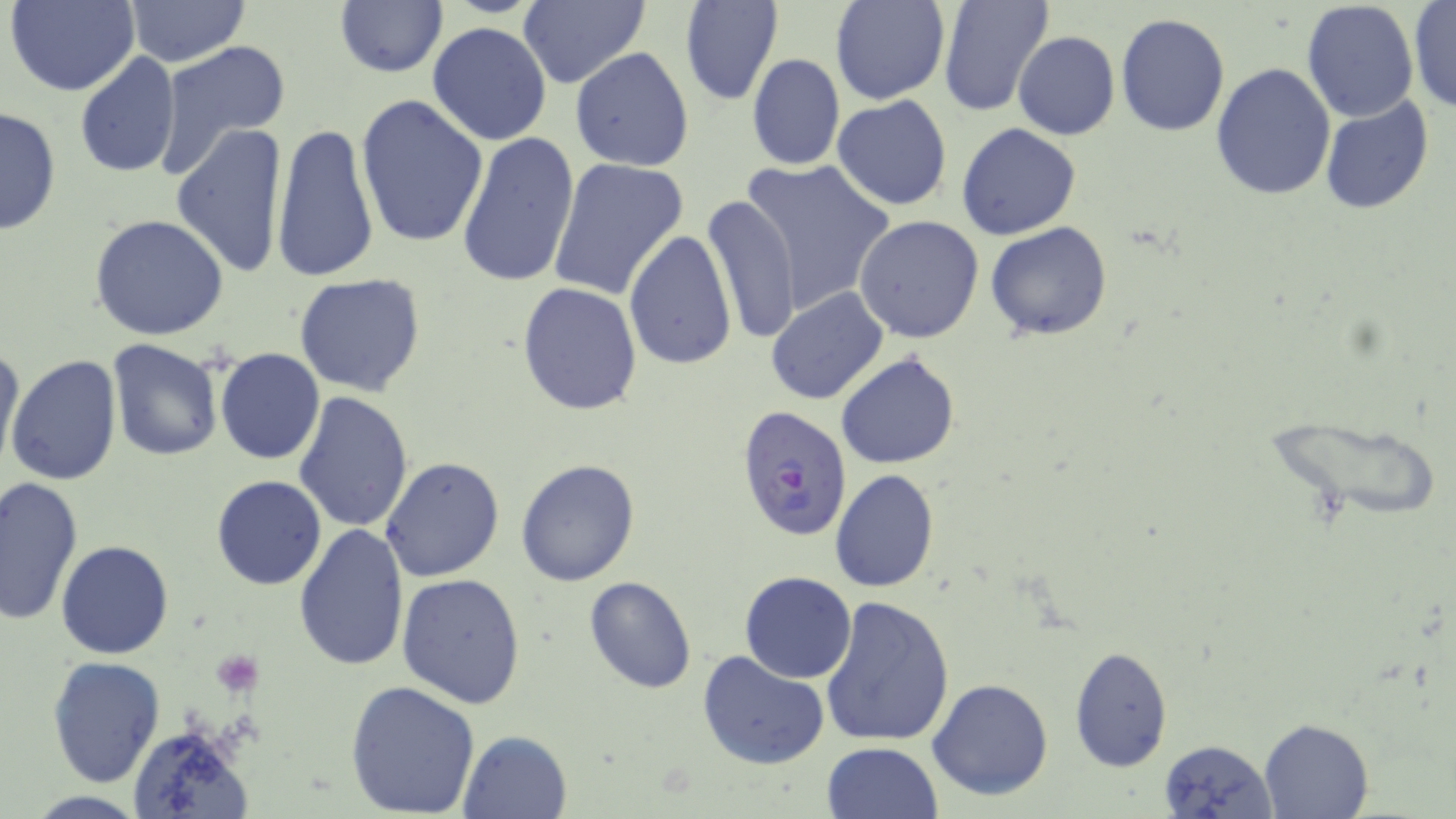

Summary:
  - Coordinate format: approximate bounding boxes as named x1/y1/x2/y2 corners in pixels
  - Plasmodium falciparum-infected red blood cell locations: (x1=734, y1=404, x2=854, y2=543)
  - Uninfected red blood cell locations: (x1=5, y1=0, x2=139, y2=96), (x1=125, y1=0, x2=248, y2=67), (x1=334, y1=0, x2=448, y2=79), (x1=680, y1=0, x2=784, y2=107), (x1=830, y1=0, x2=950, y2=105), (x1=937, y1=0, x2=1055, y2=117), (x1=1301, y1=1, x2=1418, y2=121), (x1=1408, y1=1, x2=1456, y2=114), (x1=517, y1=3, x2=652, y2=89), (x1=1115, y1=13, x2=1230, y2=136), (x1=429, y1=21, x2=551, y2=145), (x1=1013, y1=31, x2=1120, y2=141), (x1=153, y1=38, x2=291, y2=178), (x1=569, y1=47, x2=694, y2=173), (x1=75, y1=52, x2=182, y2=179), (x1=746, y1=54, x2=845, y2=171), (x1=1209, y1=61, x2=1336, y2=201), (x1=355, y1=95, x2=488, y2=249), (x1=1320, y1=95, x2=1433, y2=217), (x1=831, y1=96, x2=952, y2=211), (x1=0, y1=104, x2=62, y2=237), (x1=270, y1=121, x2=379, y2=284), (x1=170, y1=123, x2=290, y2=279), (x1=956, y1=124, x2=1081, y2=241), (x1=456, y1=130, x2=581, y2=288), (x1=547, y1=156, x2=687, y2=301), (x1=738, y1=158, x2=897, y2=316), (x1=702, y1=195, x2=801, y2=345), (x1=90, y1=215, x2=228, y2=341), (x1=854, y1=215, x2=984, y2=342), (x1=985, y1=221, x2=1112, y2=339), (x1=625, y1=230, x2=736, y2=372), (x1=293, y1=272, x2=426, y2=395), (x1=516, y1=281, x2=642, y2=416), (x1=766, y1=287, x2=889, y2=406), (x1=0, y1=339, x2=24, y2=473), (x1=107, y1=339, x2=225, y2=461), (x1=214, y1=349, x2=325, y2=465), (x1=837, y1=352, x2=960, y2=470), (x1=7, y1=356, x2=122, y2=485), (x1=293, y1=390, x2=415, y2=533), (x1=380, y1=456, x2=506, y2=582), (x1=515, y1=459, x2=640, y2=586), (x1=829, y1=470, x2=940, y2=592), (x1=211, y1=476, x2=327, y2=591), (x1=1, y1=477, x2=83, y2=624), (x1=295, y1=523, x2=409, y2=673), (x1=56, y1=538, x2=174, y2=659), (x1=738, y1=571, x2=857, y2=683), (x1=396, y1=572, x2=527, y2=709), (x1=583, y1=576, x2=698, y2=693), (x1=820, y1=596, x2=955, y2=747), (x1=1068, y1=647, x2=1173, y2=772), (x1=697, y1=650, x2=830, y2=770), (x1=46, y1=655, x2=166, y2=788), (x1=346, y1=679, x2=480, y2=817), (x1=927, y1=679, x2=1055, y2=802), (x1=1259, y1=717, x2=1374, y2=818), (x1=130, y1=725, x2=254, y2=819), (x1=459, y1=729, x2=572, y2=819), (x1=1158, y1=739, x2=1278, y2=818), (x1=821, y1=740, x2=943, y2=818)
  - Platelet locations: (x1=210, y1=652, x2=264, y2=695)
  - Slide-level diagnosis: Plasmodium falciparum
  - Field of view: single
  - Image size: 1456×819 pixels
  - Modality: optical microscopy
  - Preparation: thin blood smear
  - Stain: May-Grünwald-Giemsa
  - Magnification: 1000x